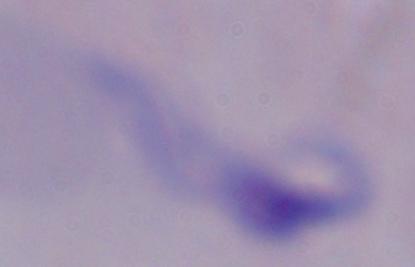 A trypanosome is shown. 1000x magnification. Photomicrograph.